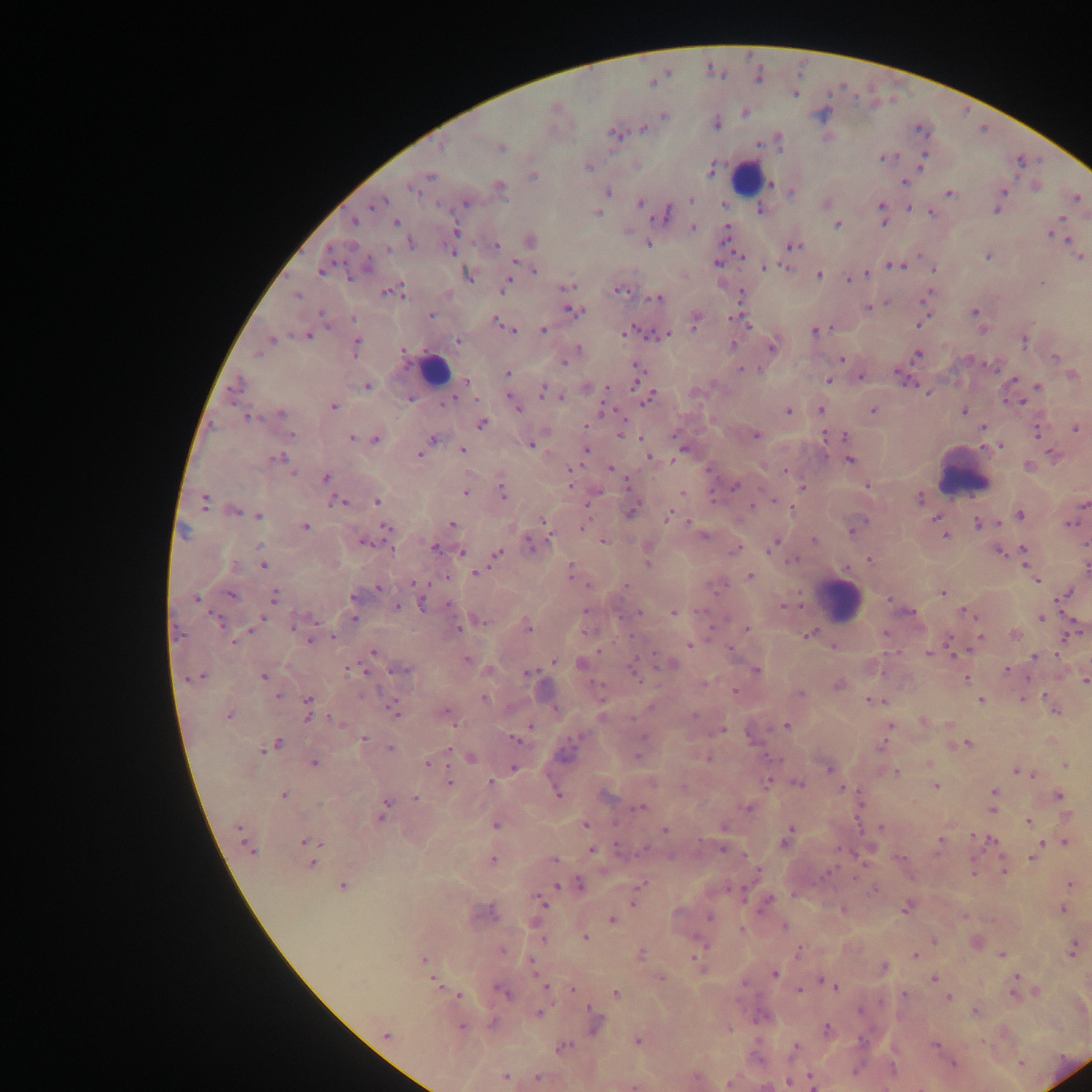
country = Ghana
preparation = thick blood film
capture = mobile-phone photograph through a microscope
leukocyte locations = approximate centers as (x, y) in pixels: (747, 176), (435, 369), (962, 473), (841, 599)
image size = 1092×1092 pixels
malaria parasite locations = approximate centers as (x, y) in pixels: (758, 77), (652, 82), (795, 95), (664, 116), (716, 123), (643, 129), (919, 130), (613, 133), (442, 145), (501, 148), (885, 158), (923, 160), (588, 167), (711, 169), (430, 176), (533, 176), (905, 183), (771, 184), (499, 186), (412, 190), (791, 191), (1003, 191), (608, 192), (950, 193), (691, 198), (1076, 198), (466, 203), (640, 203), (826, 204), (375, 205), (881, 205), (996, 210), (761, 211), (598, 213), (667, 213), (930, 213), (355, 222), (396, 223), (882, 223), (836, 225), (693, 227), (456, 230), (726, 232), (1052, 235), (530, 240), (1066, 240), (411, 243), (648, 243), (495, 245), (794, 246), (387, 249), (450, 251), (988, 256), (1079, 257), (717, 263), (367, 266), (895, 266), (766, 267), (782, 267), (932, 267), (534, 271), (322, 272), (866, 273), (349, 274), (818, 275), (467, 276), (849, 279), (1041, 283), (567, 286), (505, 287), (621, 291), (386, 292), (396, 292), (297, 295), (742, 295), (926, 297), (656, 298), (886, 303), (867, 308), (573, 310), (975, 312), (322, 314), (430, 314), (353, 319), (923, 321), (694, 322), (497, 323), (745, 323), (543, 329), (512, 330), (634, 330), (628, 331), (814, 331), (664, 335), (307, 336), (272, 340), (458, 341), (1025, 342), (356, 345), (732, 345), (771, 347), (578, 348), (403, 352), (258, 354), (918, 354), (1055, 357), (841, 358), (564, 362), (635, 368), (742, 369), (507, 374), (1072, 375), (861, 376), (1014, 380), (466, 381), (829, 381), (238, 385), (368, 386), (1038, 386), (636, 387), (541, 390), (648, 396), (563, 397), (411, 399), (449, 401), (1017, 402), (333, 406), (517, 408), (820, 409), (789, 410), (873, 411), (964, 411), (281, 414), (248, 417), (482, 424), (983, 427), (1075, 429), (1037, 432), (291, 435), (621, 435), (756, 435), (844, 435), (351, 438), (375, 439), (432, 439), (531, 444), (998, 445), (462, 450), (585, 450), (419, 454), (1053, 456), (278, 458), (648, 458), (850, 460), (1029, 465), (610, 468), (571, 471), (292, 472), (785, 472), (326, 478), (569, 484), (866, 485), (736, 486), (803, 488), (502, 491), (682, 492), (464, 493), (920, 498), (205, 501), (377, 501), (338, 502), (1083, 504), (753, 506), (631, 511), (235, 512), (1020, 514), (259, 516), (668, 516), (936, 518), (543, 520), (978, 523), (1070, 524), (452, 525), (305, 527), (386, 527), (853, 530), (703, 536), (945, 536), (603, 540), (813, 540), (363, 542), (530, 544), (772, 545), (260, 546), (434, 548), (735, 550), (1024, 550), (1001, 552), (461, 553), (497, 553), (869, 559), (794, 560), (648, 562), (234, 566), (263, 566), (1087, 568), (570, 570), (476, 573), (750, 576), (1036, 580), (415, 583), (625, 586), (378, 588), (943, 593), (232, 594), (1066, 594), (275, 596), (353, 597), (195, 599), (890, 600), (422, 604), (450, 605), (784, 606), (397, 608), (586, 611), (910, 612), (638, 613), (674, 613), (966, 613), (261, 618), (1042, 618), (354, 619), (219, 620), (481, 621), (293, 625), (528, 627), (746, 628), (457, 629), (251, 630), (177, 634), (810, 634), (885, 634), (1015, 635), (332, 636), (979, 637), (309, 641), (234, 642), (689, 644), (833, 646), (949, 647), (730, 650), (373, 652), (929, 653), (1035, 656), (468, 661), (553, 662), (580, 663), (670, 663), (349, 669), (359, 670), (403, 670), (756, 670), (1006, 670), (367, 671), (634, 673), (529, 674), (202, 676), (263, 677), (966, 679), (1085, 682), (703, 683), (838, 685), (735, 691), (800, 695), (278, 696), (484, 698), (308, 700), (875, 701), (981, 701), (1054, 711), (395, 712), (446, 712), (694, 715), (229, 716), (307, 717), (337, 721), (922, 721), (949, 724), (787, 725), (890, 726), (530, 727), (722, 731), (364, 738), (642, 738), (514, 739), (278, 743), (967, 744), (882, 746), (390, 749), (449, 749), (262, 750), (637, 757), (471, 758), (707, 759), (428, 763), (314, 764), (929, 764), (1065, 765), (515, 768), (828, 769), (896, 772), (1018, 772), (450, 782), (491, 782), (652, 783), (768, 783), (798, 784), (935, 786), (844, 789), (994, 791), (557, 793), (284, 794), (1058, 795), (606, 797), (415, 798), (320, 804), (386, 805), (641, 808), (747, 808), (993, 809), (382, 816), (1028, 820), (585, 824), (496, 825), (723, 827), (880, 827), (239, 828), (666, 831), (789, 833), (941, 840), (990, 840), (308, 841), (785, 842), (1064, 842), (1041, 844), (250, 850), (723, 850), (592, 851), (619, 852), (1034, 853), (1032, 857), (309, 859), (553, 859), (902, 859), (492, 860), (313, 864), (1003, 870), (973, 873), (579, 884), (641, 884), (1069, 884), (557, 885), (342, 887), (873, 891), (768, 900), (540, 901), (633, 904), (906, 908), (843, 909), (1063, 909), (489, 912), (710, 917), (612, 920), (784, 926), (741, 929), (586, 937), (543, 940), (934, 941), (1073, 948), (502, 950), (798, 952), (641, 953), (916, 955), (1001, 955), (424, 959), (695, 959), (531, 963), (883, 967), (774, 974), (660, 977), (1015, 978), (934, 979), (434, 982), (744, 983), (827, 983), (832, 985), (546, 988), (572, 989), (799, 990), (503, 993), (616, 994), (1014, 994), (458, 995), (905, 995), (947, 997), (860, 1011), (974, 1011), (539, 1013), (595, 1023), (492, 1024), (462, 1027), (827, 1029), (729, 1030), (386, 1035), (638, 1040), (934, 1045), (564, 1046), (795, 1047), (953, 1064), (1020, 1064), (854, 1071), (505, 1077), (538, 1077), (811, 1080), (788, 1083), (634, 1087)
field of view = single